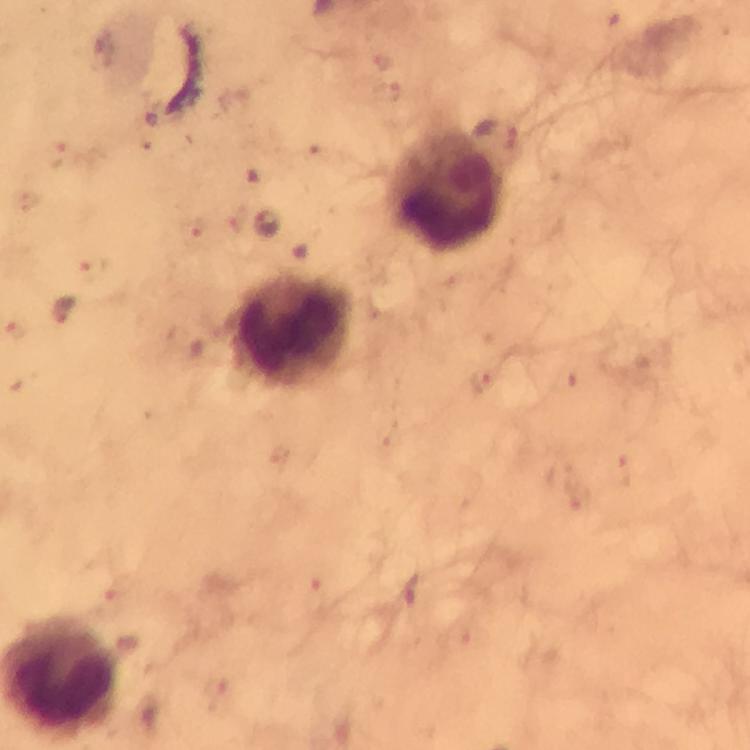
Approximate centers as {x, y} in pixels.
Summary:
  - Malaria parasite locations: {265, 223}, {61, 312}
  - Leukocyte locations: {445, 190}, {292, 329}
  - Context: from a malaria diagnostic workup
  - Magnification: 100x
  - Immersion oil: used
  - Image size: 750×750 pixels
  - Stain: Giemsa
  - Cropped from: one field of view
  - Capture: smartphone mounted on the microscope
  - Preparation: thick blood smear